Identify the preparation type.
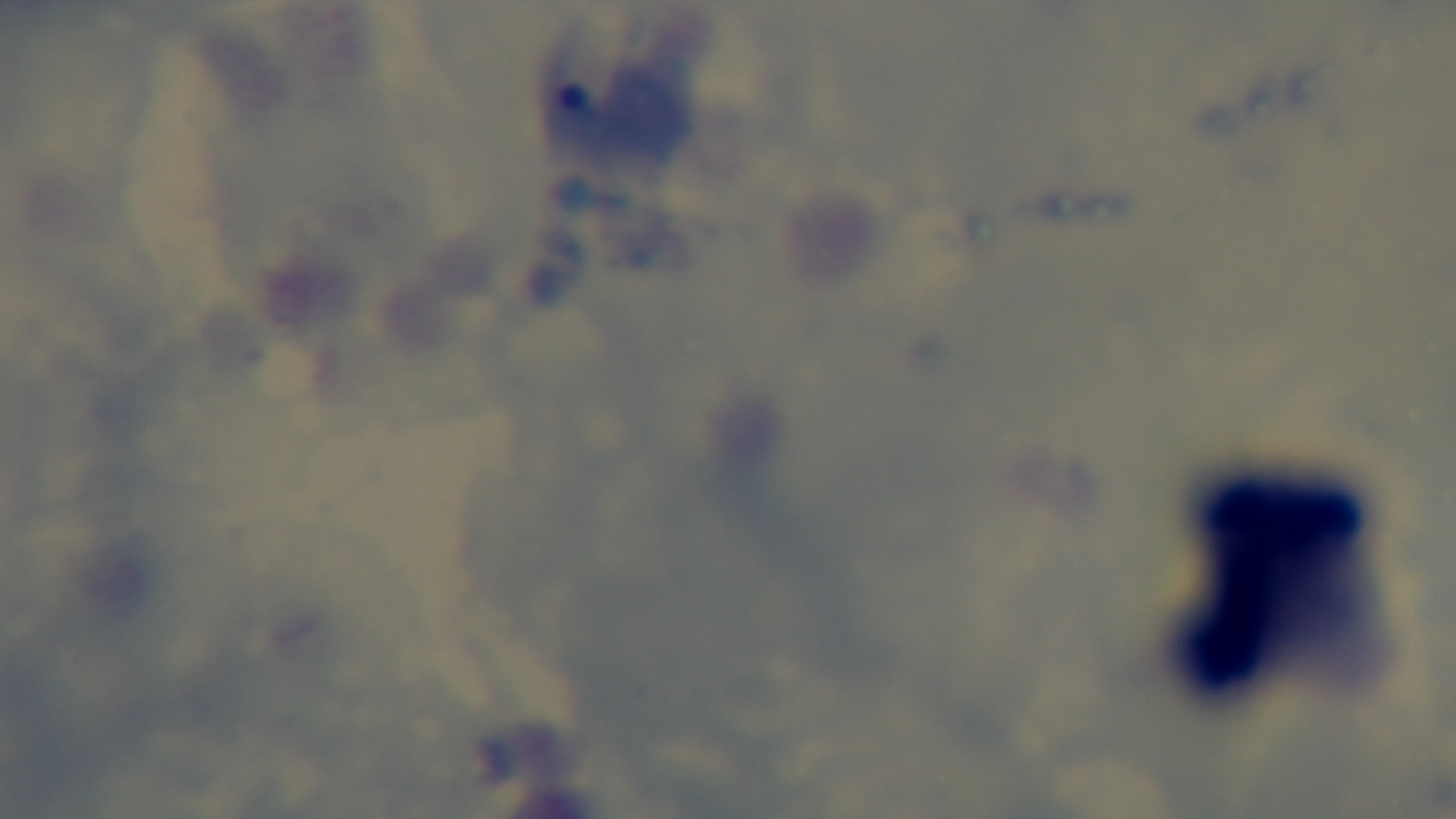
A thick smear.

modality = light microscopy
field of view = single
malaria status = negative
stain = Giemsa
objective = 100x oil immersion
capture = mounted 4K digital camera